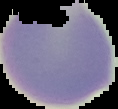

Summary:
  - Image size: 118×109 pixels
  - Image type: segmented cell region on a black background
  - Preparation: thin blood film
  - Result: negative for malaria parasites